Identify the blood parasite species.
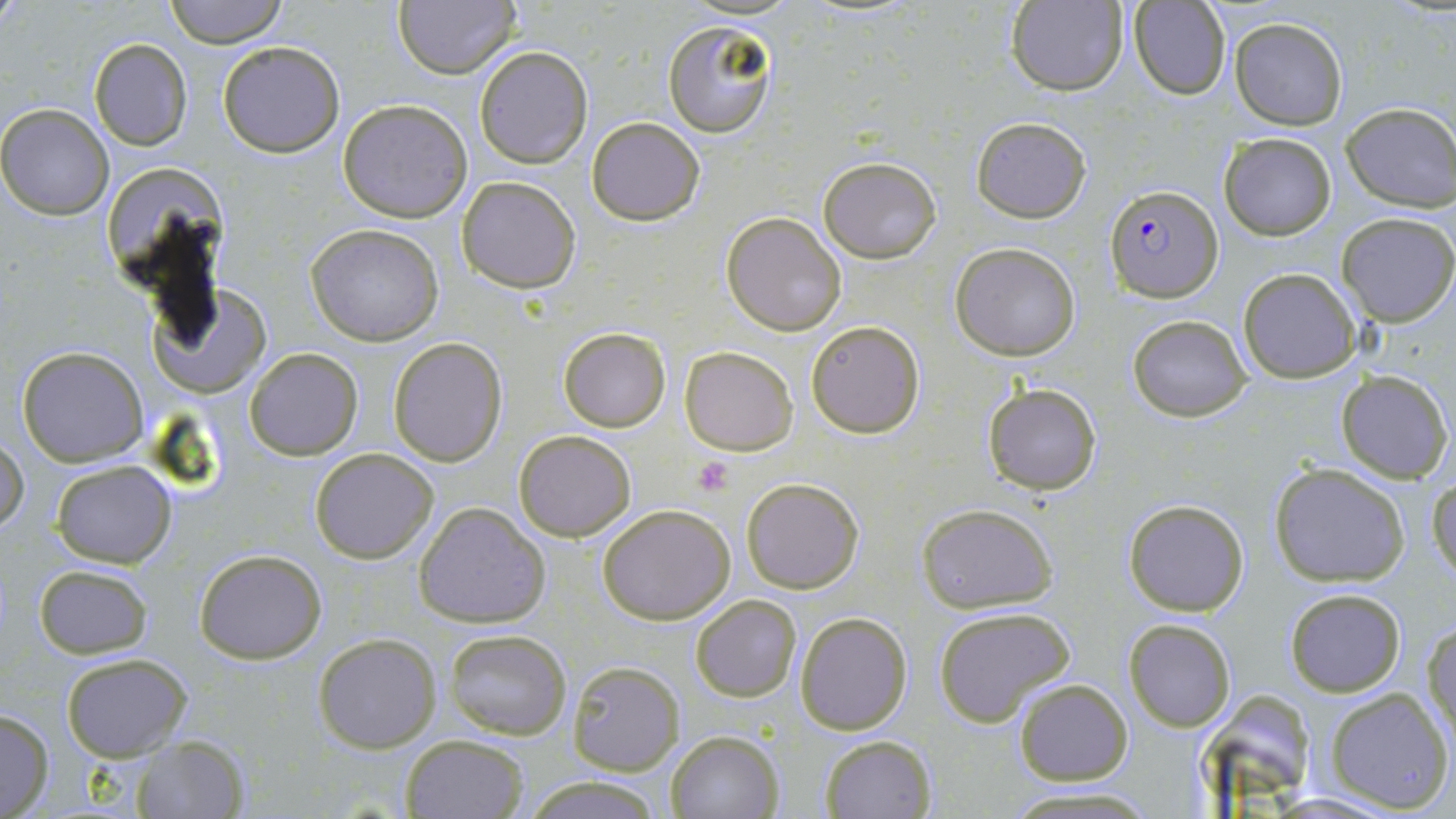

Plasmodium falciparum.

{
  "image_size": "1456×819 pixels",
  "field_of_view": "single",
  "stain": "May-Grünwald-Giemsa",
  "preparation": "thin blood film",
  "magnification": "1000x",
  "plasmodium_falciparum_infected_red_blood_cell_locations": "approximate bounding boxes as (x1,y1)-(x2,y2) corner pairs in pixels: (1105,187)-(1224,304)",
  "uninfected_red_blood_cell_locations": "approximate bounding boxes as (x1,y1)-(x2,y2) corner pairs in pixels: (164,0)-(289,48), (1004,1)-(1129,94), (1128,1)-(1227,100), (393,2)-(521,78), (1231,18)-(1347,130), (662,21)-(776,139), (88,37)-(192,150), (217,40)-(345,156), (474,46)-(592,169), (338,98)-(474,222), (1341,102)-(1456,209), (0,103)-(113,219), (969,114)-(1092,222), (586,116)-(706,225), (1222,133)-(1336,240), (817,156)-(943,262), (103,159)-(231,281), (455,174)-(582,293), (722,210)-(848,335), (1336,211)-(1455,326), (304,223)-(445,346), (950,242)-(1081,361), (1238,267)-(1361,382), (146,293)-(273,399), (1127,315)-(1252,422), (807,321)-(924,438), (558,326)-(671,432), (388,337)-(507,466), (16,346)-(148,466), (681,346)-(798,455), (244,348)-(362,460), (1334,370)-(1453,482), (981,383)-(1103,495), (513,428)-(637,542), (1,433)-(29,535), (310,447)-(438,563), (52,459)-(177,567), (1269,461)-(1412,587), (1428,474)-(1455,585), (741,477)-(864,594), (1122,497)-(1250,616), (915,501)-(1059,613), (413,502)-(550,628), (597,504)-(736,624), (193,548)-(327,663), (34,564)-(152,659), (1284,587)-(1406,696), (691,594)-(802,702), (933,605)-(1075,727), (795,610)-(912,734), (1122,617)-(1235,731), (1425,620)-(1456,750), (443,629)-(571,740), (315,634)-(440,752), (61,652)-(192,760), (567,661)-(684,774), (1014,678)-(1132,785), (1192,688)-(1317,801), (1324,688)-(1453,813), (0,707)-(53,817), (665,730)-(784,818), (398,734)-(530,818), (131,735)-(250,818), (820,735)-(938,819), (522,774)-(665,819), (1003,785)-(1158,817)",
  "modality": "light microscopy",
  "platelet_locations": "approximate bounding boxes as (x1,y1)-(x2,y2) corner pairs in pixels: (692,456)-(734,497)"
}